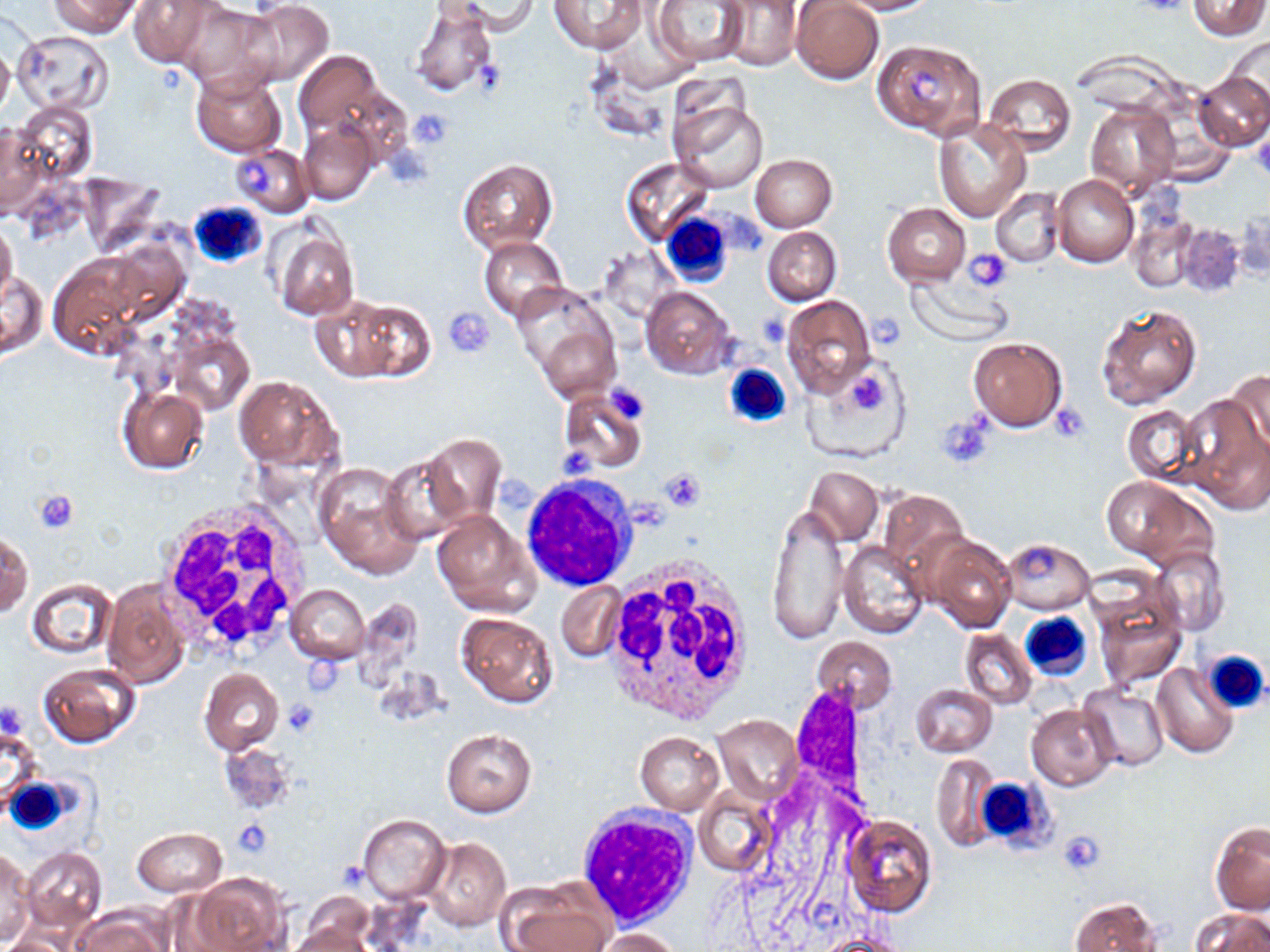
slide-level diagnosis = no evidence of blood parasites
image size = 1270×952 pixels
preparation = thin blood smear
modality = optical microscopy
platelet locations = approximate bounding boxes as [x1, y1, x2, y2] in pixels: [1133, 0, 1194, 19], [471, 59, 505, 97], [906, 68, 943, 99], [407, 109, 455, 150], [1249, 133, 1270, 179], [236, 157, 272, 195], [963, 248, 1012, 290], [446, 308, 498, 358], [758, 313, 790, 348], [868, 316, 905, 353], [847, 365, 888, 416], [602, 383, 651, 424], [1052, 404, 1091, 441], [937, 414, 995, 469], [557, 450, 599, 480], [659, 466, 707, 510], [496, 474, 538, 514], [34, 490, 79, 535], [622, 498, 668, 530], [282, 699, 322, 737], [231, 820, 272, 856], [1058, 830, 1104, 876]
white blood cell locations = approximate bounding boxes as [x1, y1, x2, y2] in pixels: [188, 200, 267, 270], [662, 211, 734, 288], [724, 363, 793, 430], [520, 476, 636, 592], [154, 498, 313, 664], [601, 557, 757, 725], [1019, 612, 1093, 680], [1200, 648, 1270, 716], [5, 774, 73, 837], [974, 776, 1056, 853], [574, 805, 695, 926]
field of view = one of a larger specimen
uninfected red blood cell locations = approximate bounding boxes as [x1, y1, x2, y2] in pixels: [52, 0, 142, 37], [130, 0, 221, 67], [436, 0, 538, 35], [650, 0, 747, 67], [829, 0, 938, 14], [1188, 0, 1268, 39], [239, 1, 335, 87], [552, 1, 646, 53], [720, 1, 804, 69], [791, 1, 884, 84], [177, 4, 280, 92], [409, 4, 498, 97], [13, 29, 113, 115], [1223, 35, 1270, 120], [871, 39, 987, 140], [0, 41, 14, 121], [581, 46, 676, 145], [294, 51, 384, 138], [190, 70, 286, 157], [1195, 72, 1270, 151], [984, 74, 1077, 153], [668, 98, 771, 196], [13, 101, 97, 188], [1087, 102, 1178, 200], [933, 118, 1030, 222], [298, 119, 378, 205], [1, 123, 50, 219], [227, 142, 313, 217], [751, 154, 836, 232], [620, 158, 714, 247], [458, 159, 557, 253], [76, 173, 168, 256], [1051, 176, 1139, 267], [990, 188, 1063, 267], [882, 203, 971, 286], [1129, 213, 1197, 293], [0, 220, 18, 310], [1175, 222, 1246, 299], [763, 226, 841, 306], [271, 227, 359, 320], [479, 236, 570, 322], [599, 247, 681, 322], [46, 252, 156, 358], [0, 271, 47, 359], [908, 275, 1012, 345], [511, 282, 621, 393], [641, 285, 736, 378], [782, 295, 875, 395], [339, 299, 436, 382], [1096, 301, 1204, 411], [169, 330, 253, 414], [969, 337, 1067, 431], [807, 355, 911, 463], [1228, 370, 1270, 457], [235, 375, 340, 472], [117, 385, 208, 475], [559, 389, 646, 473], [1178, 392, 1268, 513], [1121, 405, 1201, 485], [425, 434, 506, 522], [381, 452, 474, 546], [316, 464, 421, 575], [806, 467, 881, 544], [1101, 476, 1199, 563], [879, 491, 967, 584], [767, 499, 851, 644], [431, 510, 540, 616], [1, 532, 32, 619], [929, 534, 1016, 633], [1001, 537, 1094, 613], [839, 540, 928, 638], [1153, 549, 1229, 635], [26, 576, 117, 659], [101, 579, 188, 690], [556, 583, 626, 662], [286, 584, 369, 664], [1093, 591, 1187, 691], [456, 613, 557, 707], [960, 629, 1037, 707], [811, 636, 898, 713], [36, 662, 141, 748], [1152, 663, 1237, 757], [199, 667, 284, 754], [910, 684, 996, 756], [1080, 685, 1168, 769], [1025, 702, 1117, 790], [713, 715, 802, 804], [2, 723, 41, 816], [441, 728, 536, 817], [635, 731, 724, 815], [217, 744, 292, 814], [930, 757, 1000, 851], [693, 789, 776, 879], [357, 814, 451, 904], [843, 814, 937, 917], [1211, 822, 1270, 915], [132, 827, 226, 897], [423, 837, 512, 931], [23, 846, 106, 934], [0, 851, 36, 943], [187, 873, 287, 952], [498, 887, 608, 952], [299, 894, 376, 949], [1069, 897, 1161, 952], [75, 907, 168, 952], [1193, 908, 1269, 952], [286, 926, 377, 952], [595, 928, 681, 952], [5, 932, 71, 952], [818, 933, 910, 952]
stain = May-Grünwald-Giemsa
magnification = 1000x